Assess this cell for malaria.
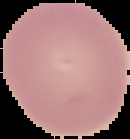
It is uninfected.

{
  "image_size": "130×139 pixels",
  "preparation": "thin blood smear",
  "image_type": "segmented cell region on a black background"
}